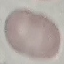
Malaria status: uninfected. Acquired by smartphone through the microscope eyepiece. Thin blood smear. Automatically extracted cell patch, resized to 64 × 64 pixels. Giemsa stain.